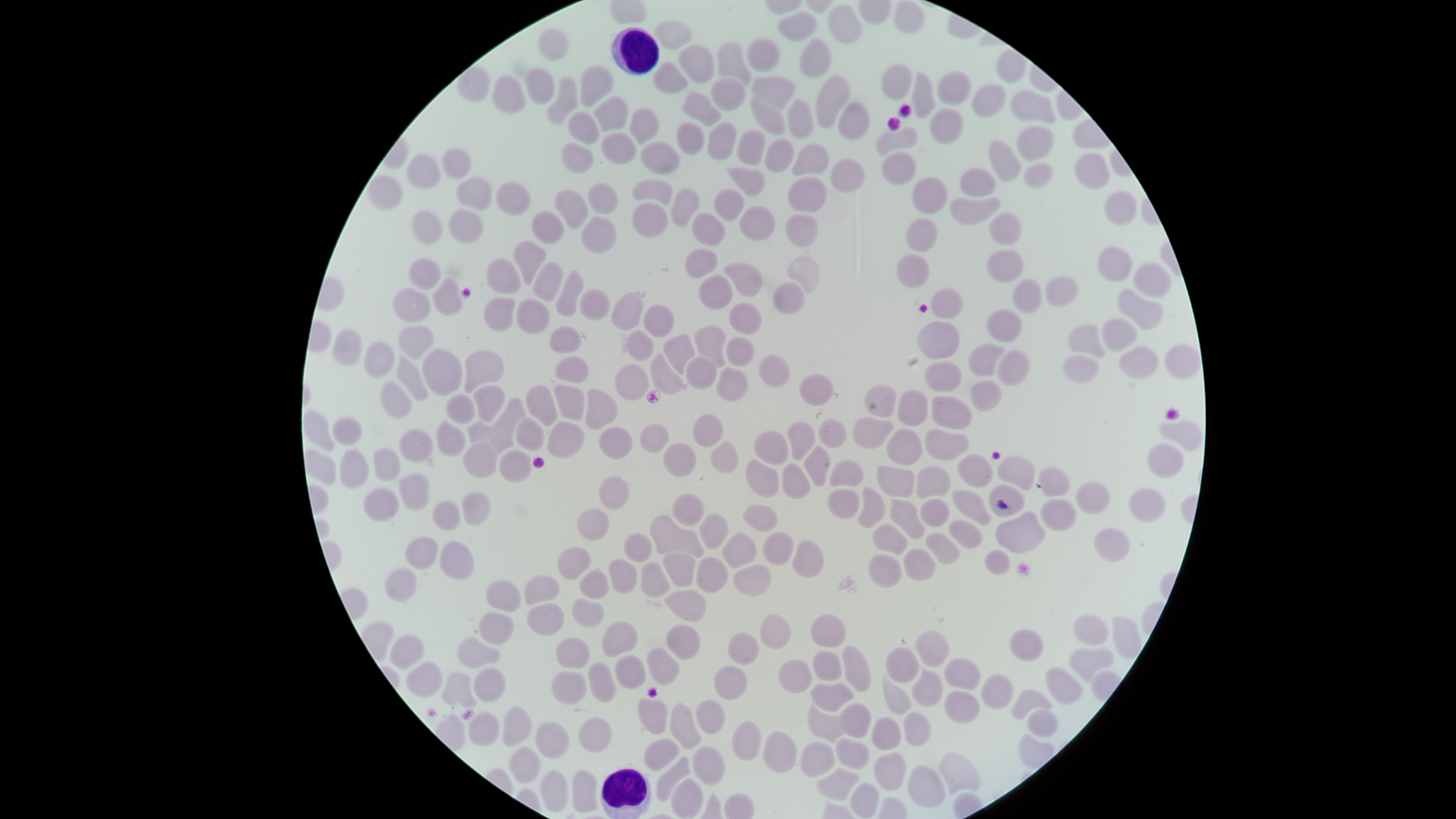
Approximate bounding boxes, in pixels from the top-left corner. Uninfected RBCs: (left=893, top=1, right=925, bottom=34), (left=827, top=3, right=862, bottom=44), (left=777, top=10, right=817, bottom=41), (left=654, top=20, right=692, bottom=50), (left=537, top=28, right=569, bottom=62), (left=746, top=37, right=780, bottom=72), (left=799, top=38, right=831, bottom=78), (left=716, top=41, right=751, bottom=86), (left=678, top=44, right=714, bottom=83), (left=996, top=49, right=1026, bottom=84), (left=652, top=61, right=688, bottom=94), (left=881, top=63, right=912, bottom=100), (left=580, top=65, right=614, bottom=108), (left=525, top=67, right=555, bottom=104), (left=936, top=70, right=971, bottom=106), (left=912, top=72, right=936, bottom=118), (left=492, top=74, right=526, bottom=114), (left=751, top=74, right=797, bottom=110), (left=815, top=74, right=851, bottom=128), (left=546, top=76, right=577, bottom=125), (left=710, top=77, right=746, bottom=111), (left=971, top=83, right=1007, bottom=117), (left=1010, top=90, right=1056, bottom=124), (left=682, top=91, right=722, bottom=128), (left=593, top=96, right=629, bottom=132), (left=751, top=97, right=784, bottom=135), (left=786, top=98, right=815, bottom=139), (left=837, top=101, right=871, bottom=140), (left=629, top=107, right=659, bottom=145), (left=567, top=111, right=599, bottom=145), (left=707, top=121, right=737, bottom=160), (left=676, top=122, right=705, bottom=155), (left=1016, top=125, right=1053, bottom=161), (left=875, top=126, right=918, bottom=156), (left=737, top=129, right=766, bottom=165), (left=601, top=132, right=636, bottom=164), (left=764, top=138, right=795, bottom=173), (left=988, top=140, right=1021, bottom=182), (left=640, top=141, right=680, bottom=174), (left=562, top=142, right=593, bottom=173), (left=791, top=143, right=830, bottom=176), (left=442, top=147, right=472, bottom=179), (left=881, top=152, right=917, bottom=185), (left=1074, top=152, right=1110, bottom=189), (left=406, top=154, right=441, bottom=190), (left=830, top=158, right=865, bottom=193), (left=1023, top=162, right=1053, bottom=189), (left=726, top=167, right=766, bottom=197), (left=958, top=168, right=996, bottom=197), (left=366, top=174, right=403, bottom=210), (left=456, top=176, right=493, bottom=211), (left=787, top=176, right=827, bottom=212), (left=912, top=176, right=948, bottom=214), (left=632, top=178, right=673, bottom=205), (left=495, top=181, right=531, bottom=216), (left=588, top=182, right=618, bottom=215), (left=671, top=188, right=700, bottom=228), (left=713, top=188, right=744, bottom=221), (left=553, top=189, right=589, bottom=229), (left=1104, top=190, right=1138, bottom=226), (left=950, top=196, right=1001, bottom=225), (left=630, top=202, right=668, bottom=237), (left=738, top=205, right=776, bottom=241), (left=448, top=209, right=484, bottom=244), (left=411, top=210, right=443, bottom=245), (left=530, top=211, right=564, bottom=244), (left=691, top=212, right=725, bottom=246), (left=989, top=212, right=1022, bottom=246), (left=785, top=214, right=819, bottom=248), (left=581, top=217, right=616, bottom=254), (left=905, top=218, right=938, bottom=252), (left=513, top=240, right=547, bottom=286), (left=1096, top=246, right=1132, bottom=282), (left=684, top=248, right=718, bottom=279), (left=986, top=248, right=1024, bottom=283), (left=896, top=253, right=930, bottom=289), (left=787, top=256, right=820, bottom=293), (left=408, top=258, right=441, bottom=290), (left=485, top=258, right=521, bottom=294), (left=532, top=262, right=564, bottom=302), (left=724, top=262, right=763, bottom=298), (left=1133, top=262, right=1172, bottom=298), (left=555, top=270, right=584, bottom=317), (left=698, top=274, right=733, bottom=309), (left=1045, top=275, right=1078, bottom=307), (left=432, top=277, right=463, bottom=316), (left=1012, top=279, right=1043, bottom=314), (left=773, top=282, right=805, bottom=315), (left=392, top=288, right=431, bottom=323), (left=579, top=289, right=610, bottom=321), (left=1117, top=289, right=1164, bottom=329), (left=610, top=290, right=646, bottom=331), (left=483, top=297, right=516, bottom=332), (left=516, top=299, right=550, bottom=335), (left=729, top=301, right=762, bottom=335), (left=643, top=304, right=675, bottom=338), (left=987, top=309, right=1023, bottom=343), (left=1102, top=317, right=1137, bottom=352), (left=1068, top=323, right=1105, bottom=359), (left=397, top=324, right=434, bottom=360), (left=693, top=325, right=726, bottom=368), (left=548, top=326, right=582, bottom=354), (left=332, top=328, right=362, bottom=367), (left=621, top=330, right=654, bottom=361), (left=663, top=334, right=695, bottom=375), (left=725, top=336, right=755, bottom=367), (left=364, top=341, right=395, bottom=378), (left=968, top=343, right=1005, bottom=377), (left=1164, top=344, right=1200, bottom=380), (left=1119, top=346, right=1158, bottom=379), (left=421, top=349, right=463, bottom=396), (left=464, top=349, right=505, bottom=393), (left=997, top=350, right=1030, bottom=386), (left=650, top=353, right=687, bottom=396), (left=759, top=354, right=791, bottom=388), (left=396, top=355, right=429, bottom=401), (left=554, top=355, right=589, bottom=383), (left=1062, top=355, right=1099, bottom=384), (left=685, top=356, right=717, bottom=390), (left=924, top=361, right=962, bottom=392), (left=614, top=364, right=649, bottom=401), (left=716, top=367, right=749, bottom=402), (left=798, top=373, right=835, bottom=406), (left=971, top=380, right=1002, bottom=412), (left=379, top=382, right=412, bottom=419), (left=473, top=384, right=505, bottom=423), (left=525, top=384, right=558, bottom=427), (left=553, top=384, right=585, bottom=421), (left=864, top=384, right=897, bottom=417), (left=585, top=388, right=618, bottom=431), (left=897, top=389, right=929, bottom=427), (left=445, top=394, right=476, bottom=424), (left=931, top=395, right=973, bottom=430), (left=493, top=397, right=525, bottom=439), (left=303, top=410, right=336, bottom=452), (left=692, top=413, right=723, bottom=448), (left=515, top=416, right=544, bottom=452), (left=332, top=417, right=363, bottom=446), (left=852, top=417, right=894, bottom=449), (left=435, top=419, right=465, bottom=457), (left=818, top=419, right=847, bottom=448), (left=1159, top=419, right=1203, bottom=451), (left=467, top=421, right=514, bottom=454), (left=546, top=421, right=585, bottom=459), (left=787, top=421, right=815, bottom=461), (left=640, top=423, right=669, bottom=453), (left=599, top=426, right=633, bottom=460), (left=398, top=428, right=434, bottom=463), (left=753, top=429, right=788, bottom=465), (left=886, top=429, right=923, bottom=466), (left=925, top=429, right=970, bottom=461), (left=462, top=439, right=498, bottom=479), (left=710, top=440, right=739, bottom=474), (left=662, top=443, right=697, bottom=478), (left=1147, top=443, right=1184, bottom=478), (left=803, top=445, right=830, bottom=487), (left=339, top=448, right=370, bottom=489), (left=373, top=448, right=400, bottom=481), (left=305, top=449, right=336, bottom=486), (left=498, top=450, right=532, bottom=483), (left=958, top=454, right=993, bottom=488), (left=997, top=456, right=1035, bottom=491), (left=745, top=458, right=779, bottom=498), (left=829, top=459, right=864, bottom=487), (left=781, top=463, right=811, bottom=499), (left=876, top=465, right=915, bottom=498), (left=916, top=465, right=951, bottom=499), (left=1038, top=467, right=1071, bottom=497), (left=398, top=473, right=431, bottom=511), (left=598, top=476, right=630, bottom=510), (left=1075, top=481, right=1111, bottom=514), (left=988, top=484, right=1026, bottom=517), (left=858, top=486, right=886, bottom=529), (left=363, top=487, right=399, bottom=522), (left=827, top=488, right=860, bottom=520), (left=1129, top=488, right=1165, bottom=522), (left=951, top=490, right=991, bottom=526), (left=461, top=491, right=491, bottom=526), (left=672, top=493, right=704, bottom=526), (left=920, top=498, right=950, bottom=527), (left=1040, top=498, right=1076, bottom=532), (left=890, top=499, right=925, bottom=540), (left=432, top=500, right=461, bottom=531), (left=742, top=504, right=778, bottom=531), (left=576, top=508, right=610, bottom=542), (left=995, top=511, right=1046, bottom=553), (left=699, top=512, right=728, bottom=549), (left=649, top=515, right=704, bottom=558), (left=947, top=519, right=983, bottom=549), (left=872, top=524, right=908, bottom=555), (left=1094, top=527, right=1131, bottom=563), (left=762, top=531, right=794, bottom=565), (left=721, top=532, right=758, bottom=568), (left=925, top=532, right=961, bottom=565), (left=623, top=533, right=652, bottom=564), (left=404, top=536, right=438, bottom=570), (left=439, top=540, right=475, bottom=581), (left=792, top=540, right=824, bottom=578), (left=557, top=546, right=591, bottom=580), (left=903, top=547, right=936, bottom=581), (left=984, top=549, right=1011, bottom=575), (left=662, top=552, right=695, bottom=587), (left=868, top=554, right=902, bottom=588), (left=695, top=557, right=728, bottom=593), (left=608, top=559, right=637, bottom=593), (left=641, top=562, right=670, bottom=598), (left=733, top=564, right=771, bottom=597), (left=384, top=568, right=417, bottom=602), (left=578, top=568, right=609, bottom=600), (left=524, top=575, right=560, bottom=605), (left=486, top=579, right=521, bottom=612), (left=664, top=589, right=707, bottom=622), (left=571, top=598, right=605, bottom=628), (left=527, top=603, right=565, bottom=636), (left=478, top=612, right=514, bottom=646), (left=760, top=613, right=791, bottom=649), (left=810, top=614, right=846, bottom=647), (left=1072, top=614, right=1108, bottom=645), (left=1111, top=616, right=1142, bottom=660), (left=601, top=620, right=638, bottom=658), (left=665, top=624, right=701, bottom=660), (left=1008, top=628, right=1043, bottom=661), (left=915, top=630, right=950, bottom=667), (left=727, top=633, right=759, bottom=665), (left=389, top=634, right=424, bottom=669), (left=457, top=637, right=501, bottom=668), (left=555, top=637, right=590, bottom=669), (left=842, top=645, right=872, bottom=692), (left=885, top=647, right=919, bottom=683), (left=645, top=648, right=680, bottom=686), (left=1069, top=648, right=1114, bottom=681), (left=812, top=650, right=843, bottom=681), (left=614, top=655, right=646, bottom=689), (left=943, top=657, right=981, bottom=690), (left=778, top=659, right=813, bottom=694), (left=406, top=661, right=443, bottom=698), (left=587, top=662, right=617, bottom=703), (left=714, top=665, right=747, bottom=700), (left=473, top=667, right=506, bottom=702), (left=911, top=667, right=943, bottom=707), (left=1045, top=667, right=1082, bottom=705), (left=550, top=671, right=587, bottom=705), (left=441, top=672, right=477, bottom=707), (left=980, top=674, right=1014, bottom=709), (left=882, top=675, right=911, bottom=715), (left=810, top=682, right=854, bottom=712), (left=1011, top=689, right=1052, bottom=720), (left=944, top=690, right=980, bottom=724), (left=637, top=697, right=667, bottom=734), (left=695, top=699, right=726, bottom=736), (left=669, top=702, right=702, bottom=750), (left=839, top=702, right=872, bottom=739), (left=502, top=704, right=532, bottom=746), (left=807, top=704, right=846, bottom=743), (left=1027, top=709, right=1058, bottom=737), (left=468, top=711, right=500, bottom=745), (left=904, top=711, right=931, bottom=746), (left=579, top=716, right=613, bottom=752), (left=870, top=716, right=901, bottom=750), (left=731, top=720, right=762, bottom=761), (left=535, top=721, right=569, bottom=758), (left=763, top=731, right=797, bottom=774), (left=643, top=737, right=679, bottom=772), (left=836, top=737, right=870, bottom=770), (left=800, top=740, right=835, bottom=778), (left=692, top=745, right=726, bottom=785), (left=509, top=746, right=541, bottom=783), (left=874, top=751, right=906, bottom=791), (left=939, top=751, right=982, bottom=795), (left=656, top=755, right=690, bottom=802), (left=907, top=764, right=945, bottom=808), (left=816, top=768, right=859, bottom=801), (left=540, top=769, right=568, bottom=812), (left=571, top=769, right=597, bottom=813), (left=671, top=778, right=704, bottom=819), (left=850, top=782, right=879, bottom=817). WBCs: (left=610, top=27, right=659, bottom=75), (left=600, top=767, right=651, bottom=819). Single field of view. Giemsa-stained preparation. Presence: no malaria parasites detected. The visible region is circular. Photographed with a smartphone camera through the microscope eyepiece. Image is 1456×819 pixels. Thin blood film.